Identify the cell.
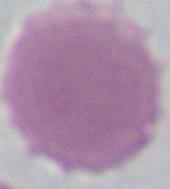

An erythrocyte.

modality: micrograph
magnification: 1000x